Classify this cell by malaria status.
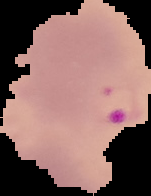

Parasitized.

image type = cell region segmented out of the field of view; surrounding area masked to black
preparation = thin blood smear
image size = 151×196 pixels